Classify this cell by malaria status.
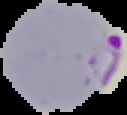
Parasitized.

Summary:
  - Preparation: thin blood smear
  - Image type: cell region segmented out of the field of view; surrounding area masked to black
  - Image size: 127×115 pixels